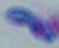

Toxoplasma gondii is shown. Captured at 1000x magnification. Photomicrograph.